Assess this cell for malaria.
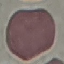
It is uninfected.

Automatically extracted cell patch, resized to 64 × 64 pixels. Photographed with a smartphone camera at the microscope eyepiece. Thin smear of blood. Giemsa stain.